Report the malaria status of this cell.
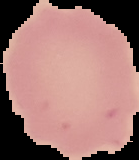

Uninfected.

From a thin blood film. The area outside the segmented cell region is set to black. Image is 139×160 pixels.